Assess this cell for malaria.
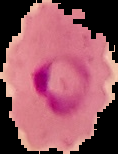

It is parasitized.

Summary:
  - Image type: cell region segmented out of the field of view; surrounding area masked to black
  - Preparation: thin blood smear
  - Image size: 118×154 pixels